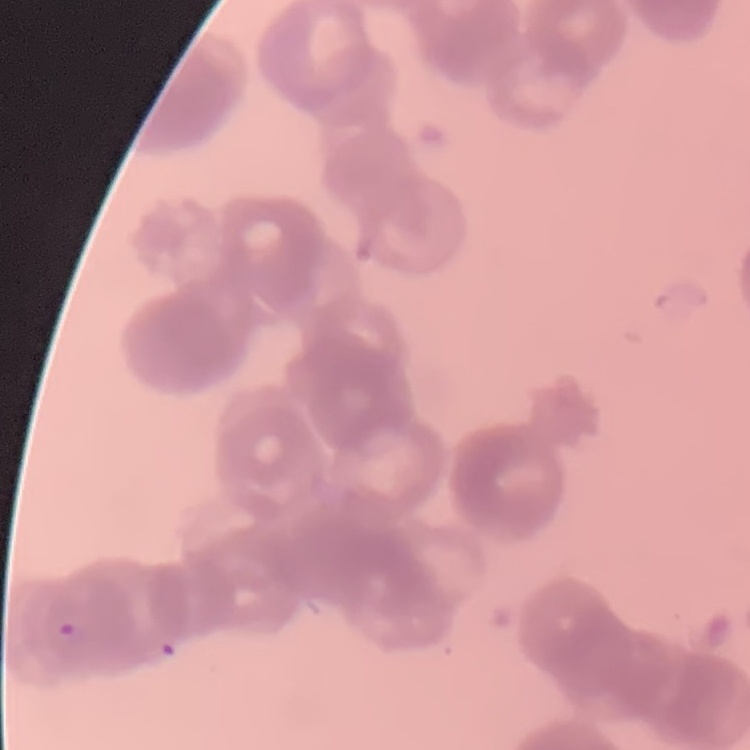

red blood cell morphology = rouleaux formation
stain = Field's or Giemsa
image type = one tile cut from a larger photomicrograph
preparation = thin blood film